Name the parasite shown.
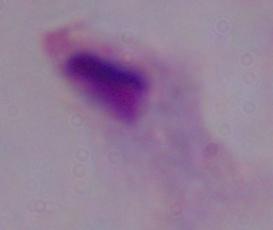
A trichomonad.

modality = micrograph
magnification = 1000x